State the blood parasite species.
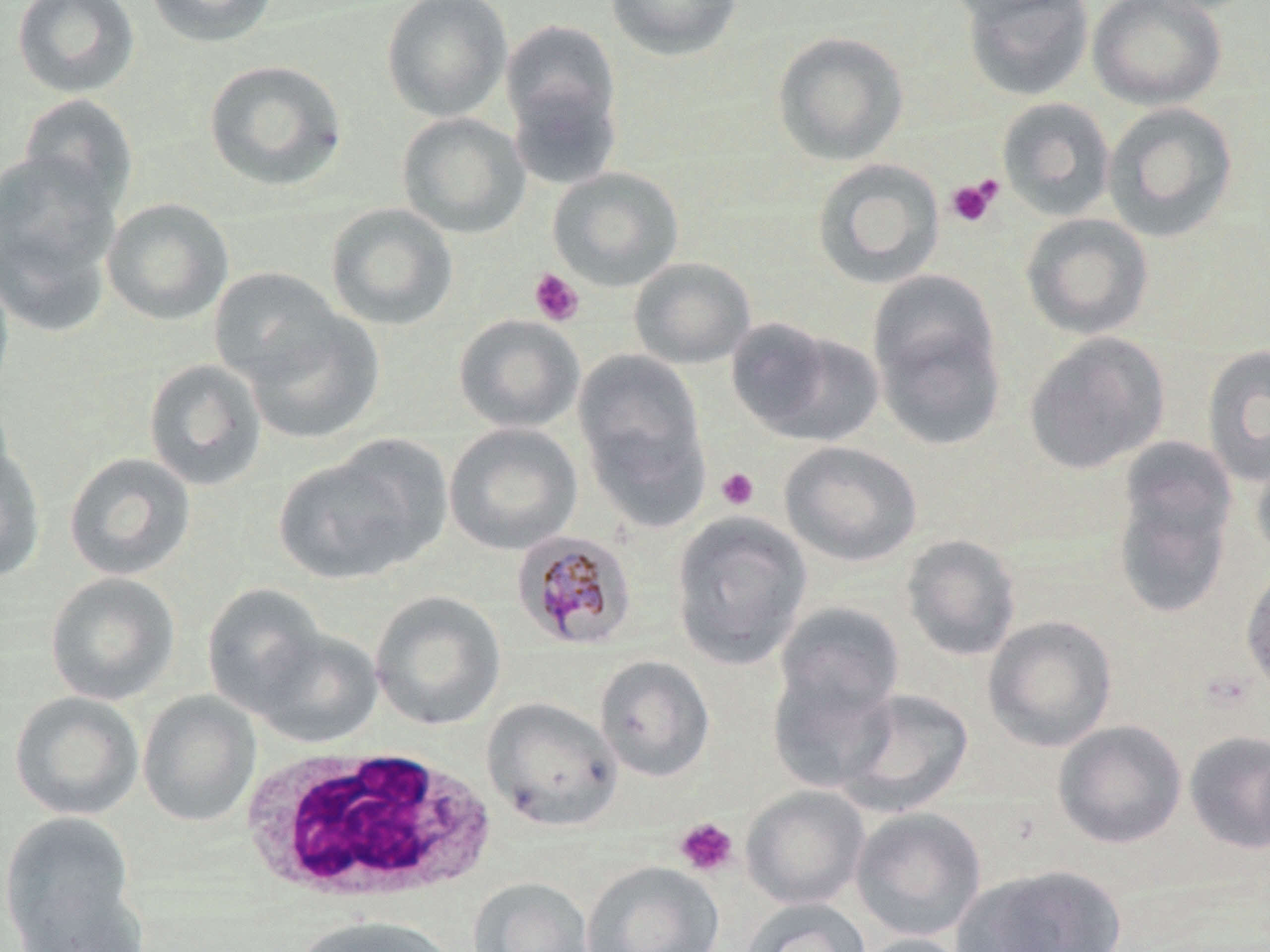

Plasmodium malariae.

Summary:
  - Coordinate format: approximate bounding boxes as named x1/y1/x2/y2 corners in pixels
  - Plasmodium malariae-infected red blood cell locations: (x1=511, y1=528, x2=638, y2=651)
  - Platelet locations: (x1=945, y1=178, x2=1001, y2=228), (x1=529, y1=268, x2=585, y2=327), (x1=715, y1=467, x2=760, y2=511), (x1=674, y1=817, x2=739, y2=877)
  - White blood cell locations: (x1=241, y1=746, x2=496, y2=906)
  - Uninfected red blood cell locations: (x1=11, y1=0, x2=141, y2=98), (x1=144, y1=0, x2=279, y2=47), (x1=381, y1=0, x2=513, y2=122), (x1=604, y1=0, x2=743, y2=61), (x1=960, y1=0, x2=1095, y2=101), (x1=1087, y1=0, x2=1227, y2=110), (x1=500, y1=19, x2=622, y2=139), (x1=772, y1=30, x2=909, y2=166), (x1=203, y1=59, x2=348, y2=191), (x1=506, y1=76, x2=623, y2=191), (x1=17, y1=93, x2=139, y2=216), (x1=996, y1=97, x2=1116, y2=221), (x1=1102, y1=102, x2=1239, y2=242), (x1=396, y1=112, x2=530, y2=239), (x1=0, y1=151, x2=123, y2=323), (x1=811, y1=158, x2=946, y2=290), (x1=548, y1=166, x2=684, y2=291), (x1=101, y1=197, x2=234, y2=326), (x1=325, y1=203, x2=459, y2=331), (x1=1020, y1=213, x2=1154, y2=340), (x1=629, y1=257, x2=756, y2=369), (x1=0, y1=265, x2=14, y2=405), (x1=208, y1=267, x2=343, y2=388), (x1=870, y1=291, x2=1006, y2=451), (x1=241, y1=306, x2=385, y2=445), (x1=453, y1=314, x2=585, y2=433), (x1=728, y1=320, x2=881, y2=445), (x1=1023, y1=331, x2=1170, y2=474), (x1=1202, y1=344, x2=1270, y2=487), (x1=574, y1=350, x2=706, y2=485), (x1=142, y1=358, x2=267, y2=492), (x1=444, y1=423, x2=583, y2=555), (x1=1109, y1=440, x2=1238, y2=618), (x1=780, y1=441, x2=923, y2=567), (x1=0, y1=443, x2=46, y2=584), (x1=273, y1=448, x2=433, y2=585), (x1=1251, y1=448, x2=1270, y2=566), (x1=64, y1=452, x2=196, y2=581), (x1=669, y1=511, x2=812, y2=669), (x1=901, y1=534, x2=1022, y2=662), (x1=1239, y1=561, x2=1270, y2=699), (x1=44, y1=571, x2=181, y2=706), (x1=202, y1=583, x2=327, y2=716), (x1=370, y1=591, x2=506, y2=731), (x1=773, y1=601, x2=906, y2=729), (x1=983, y1=615, x2=1117, y2=751), (x1=253, y1=627, x2=383, y2=749), (x1=594, y1=655, x2=716, y2=783), (x1=767, y1=657, x2=899, y2=791), (x1=835, y1=687, x2=974, y2=817), (x1=137, y1=690, x2=261, y2=827), (x1=9, y1=691, x2=144, y2=821), (x1=482, y1=696, x2=622, y2=832), (x1=1053, y1=720, x2=1187, y2=849), (x1=1183, y1=729, x2=1270, y2=855), (x1=741, y1=785, x2=870, y2=909), (x1=850, y1=806, x2=987, y2=942), (x1=0, y1=811, x2=139, y2=949), (x1=581, y1=860, x2=724, y2=952), (x1=957, y1=863, x2=1128, y2=952), (x1=467, y1=877, x2=594, y2=952), (x1=11, y1=879, x2=147, y2=952), (x1=741, y1=898, x2=871, y2=952), (x1=293, y1=915, x2=456, y2=952), (x1=852, y1=933, x2=975, y2=952)
  - Stain: May-Grünwald-Giemsa
  - Modality: light microscopy
  - Magnification: 1000x
  - Field of view: one of a larger specimen
  - Image size: 1270×952 pixels
  - Preparation: thin blood smear